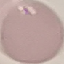
Summary:
  - Malaria status: uninfected
  - Preparation: thin blood smear
  - Image type: automatically extracted cell patch, resized to 64 × 64 pixels
  - Stain: Giemsa
  - Capture: smartphone through the microscope eyepiece